Locate every malaria parasite.
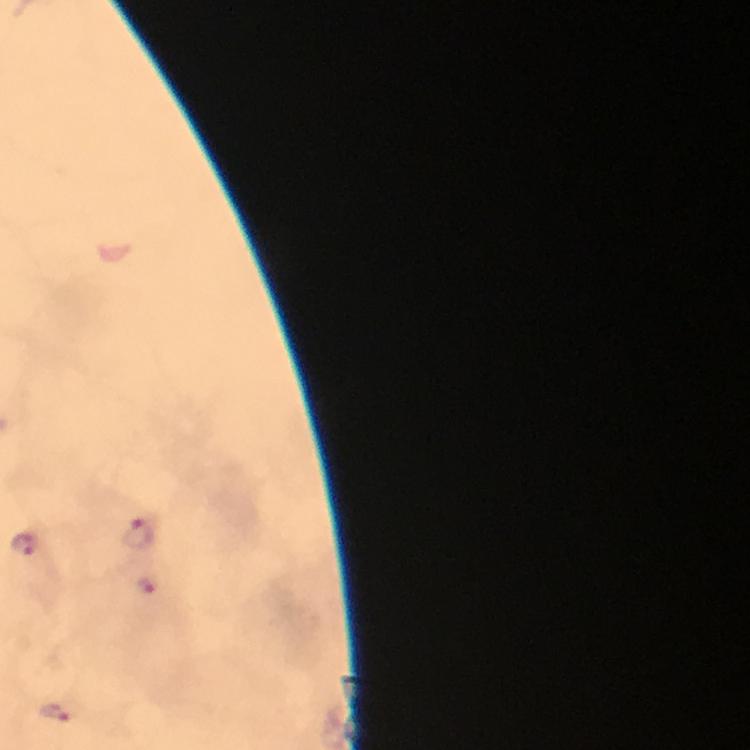

Approximate centers as [x, y] in pixels.
Malaria parasites: [138, 532], [24, 545], [145, 582], [56, 712].

Thick smear. Image is 750×750 pixels. Immersion oil applied. Giemsa stain. Photographed with a smartphone mounted on the microscope. From a diagnostic examination for malaria. Cropped region of a single field of view. 100x magnification.